Report the malaria status of this cell.
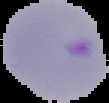

It is parasitized.

image size = 109×103 pixels
preparation = thin blood film
image type = cell region segmented out of the field of view; surrounding area masked to black